Locate every leukocyte (white blood cell).
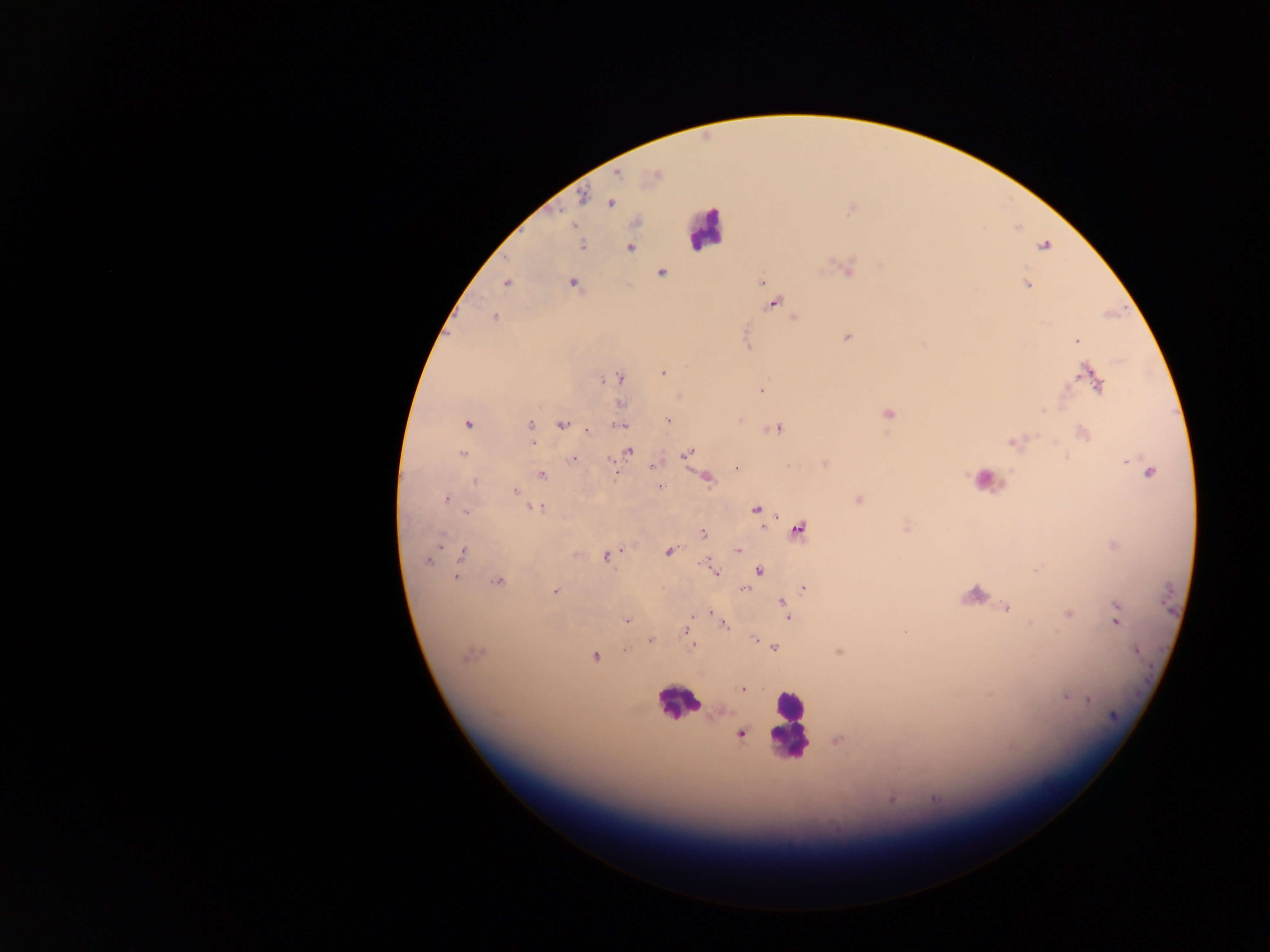
Approximate centers as x y in pixels.
Leukocytes: 703 227; 988 477; 675 702; 791 725.

capture = mobile-phone photograph through a microscope
field of view = single
country = Ghana
preparation = thick blood film
Plasmodium parasite locations = approximate centers as x y in pixels: 617 175; 583 196; 610 203; 581 245; 1045 246; 630 247; 662 273; 761 281; 506 283; 574 284; 1027 284; 773 303; 494 317; 795 318; 847 337; 1077 340; 663 372; 1089 375; 619 378; 612 379; 1097 383; 761 390; 620 404; 1043 411; 889 414; 668 421; 468 424; 531 424; 562 424; 620 425; 778 429; 587 430; 1083 433; 533 442; 1013 442; 628 452; 687 452; 462 453; 572 458; 653 467; 736 468; 1148 472; 541 475; 707 478; 475 482; 661 487; 516 491; 445 500; 858 500; 536 508; 756 510; 466 512; 799 529; 703 533; 1114 546; 738 550; 669 551; 463 552; 576 555; 607 557; 427 561; 704 562; 759 571; 1035 571; 716 573; 456 577; 497 581; 745 588; 804 588; 555 592; 782 602; 1116 606; 1006 608; 711 613; 1068 613; 692 616; 789 618; 626 620; 1116 620; 725 625; 684 632; 904 632; 755 640; 650 641; 692 645; 774 647; 626 650; 1136 650; 838 652; 469 655; 594 657; 742 689; 1065 697; 1088 699; 740 734; 891 799; 935 799
image size = 1270×952 pixels